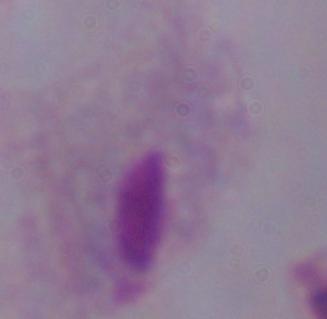

A trichomonad is shown. Photomicrograph. Captured at 1000x magnification.